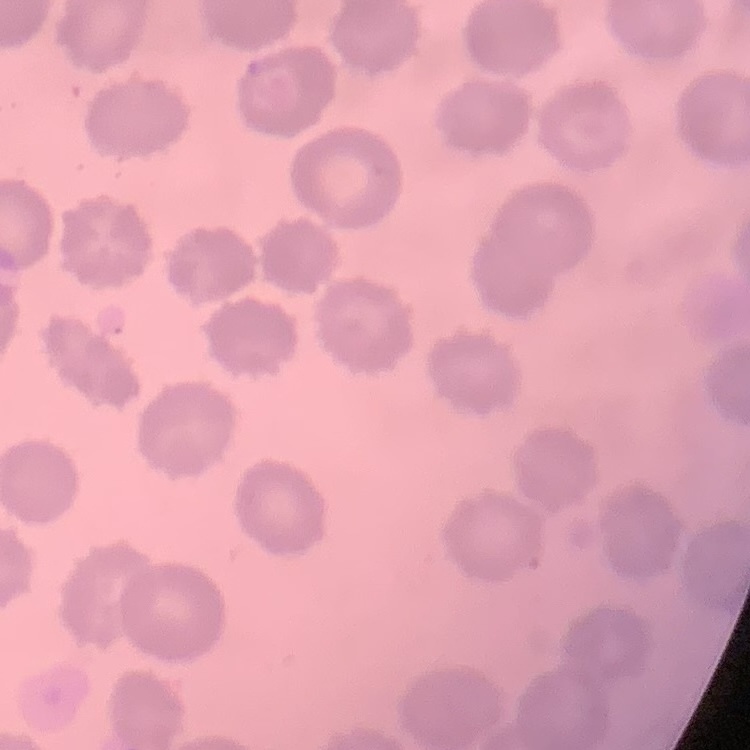
The red blood cells show no rouleaux formation. Field's or Giemsa stain. One tile cut from a larger photomicrograph. Thin blood smear.